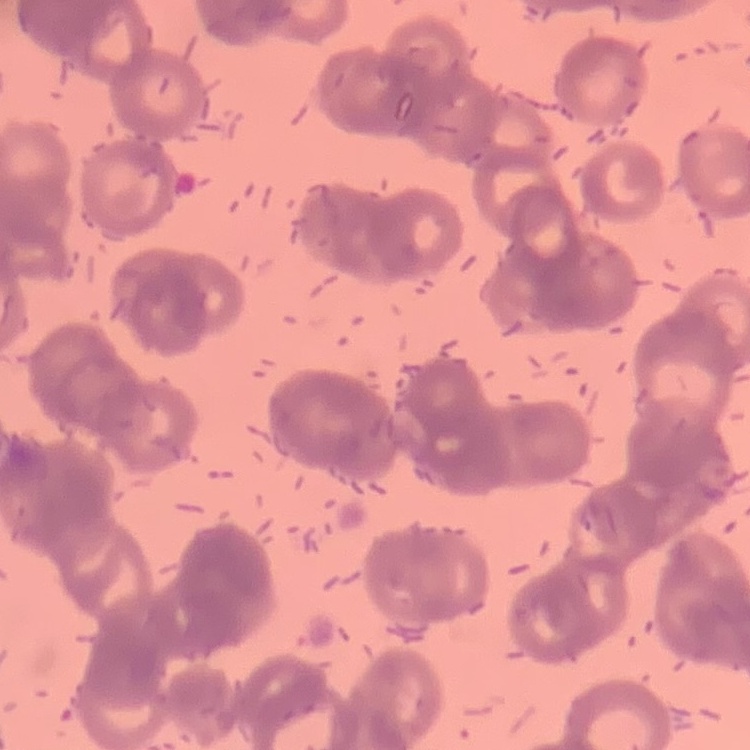
Summary:
  - Erythrocyte morphology: rouleaux formation
  - Image type: square crop of a larger photomicrograph
  - Stain: Field's or Giemsa
  - Preparation: thin blood film